Give the position of every leukocyte visible.
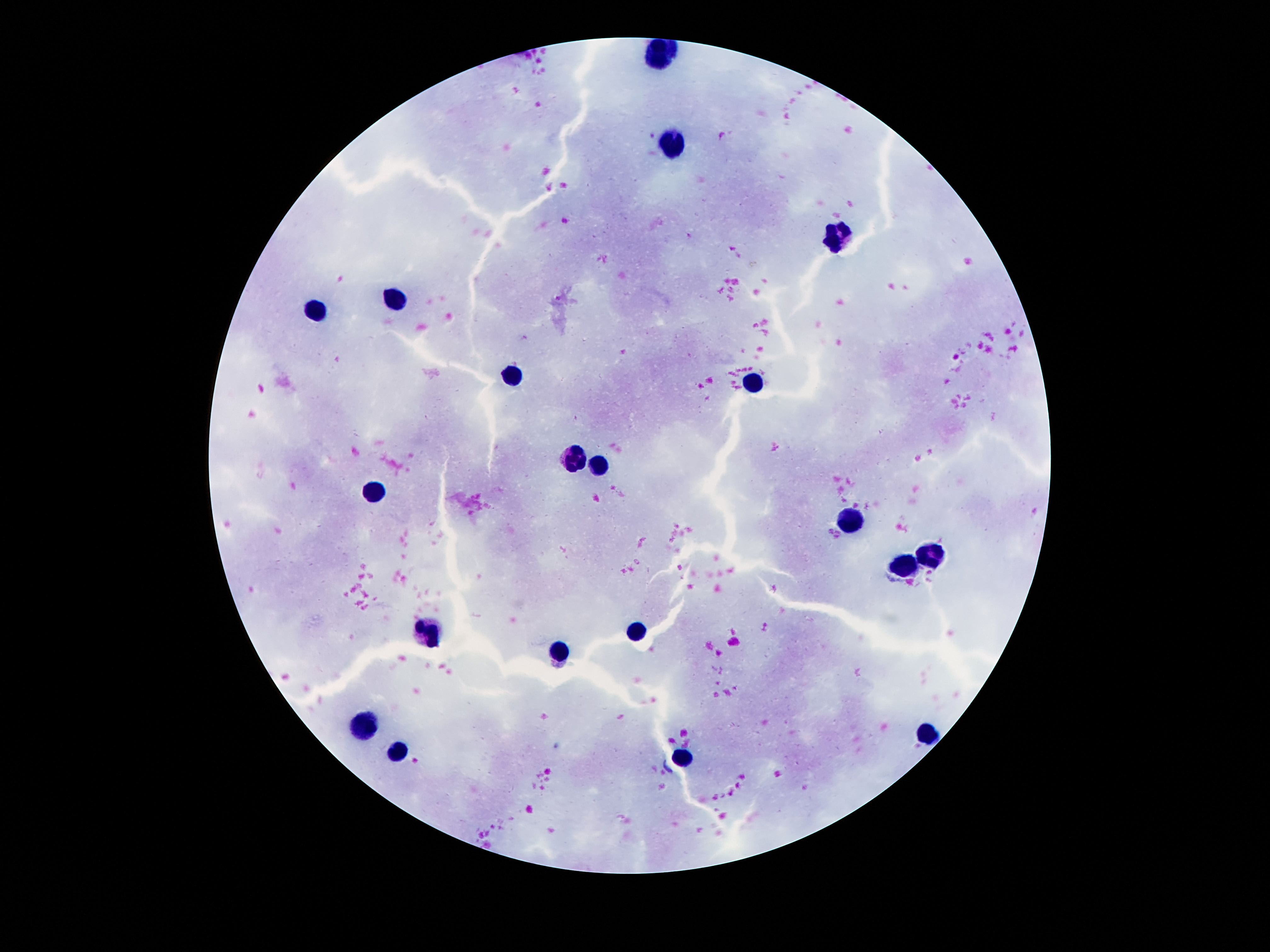
Approximate object centers, in pixels from the top-left corner.
Leukocytes: (x=661, y=54), (x=673, y=143), (x=836, y=234), (x=393, y=302), (x=316, y=311), (x=512, y=377), (x=752, y=383), (x=574, y=460), (x=603, y=468), (x=371, y=492), (x=845, y=518), (x=931, y=555), (x=906, y=568), (x=637, y=628), (x=432, y=632), (x=560, y=654), (x=364, y=726), (x=927, y=731), (x=399, y=751), (x=684, y=757).

capture = smartphone camera through the microscope eyepiece
field of view = one from this slide
image size = 1270×952 pixels
patient malaria status = negative
preparation = thick peripheral-blood smear
magnification = 100x
stain = Giemsa